Identify the cell.
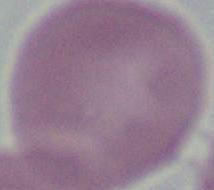

This is an erythrocyte.

modality = photomicrograph
magnification = 1000x